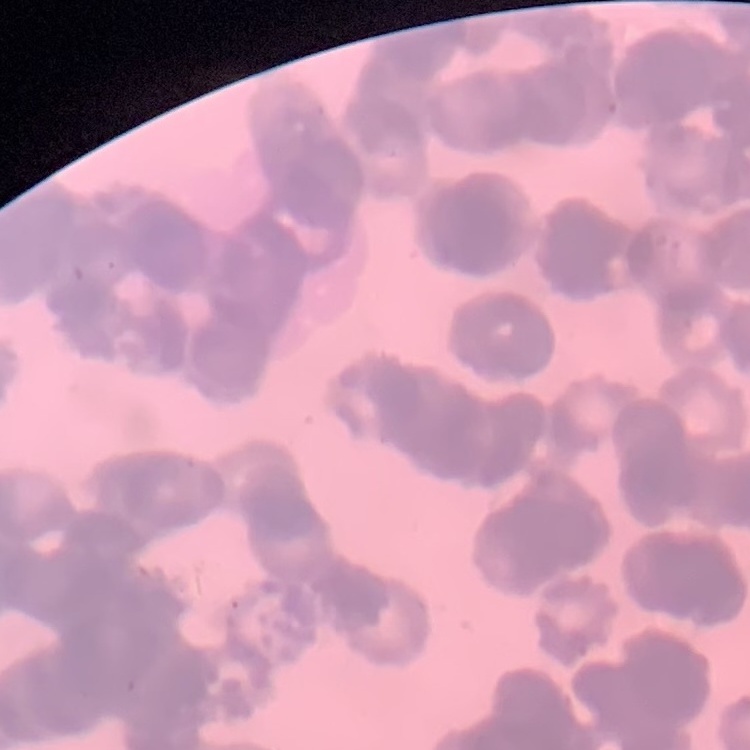

red blood cell morphology = rouleaux formation
stain = Field's or Giemsa
preparation = thin blood smear
image type = square crop of a larger photomicrograph